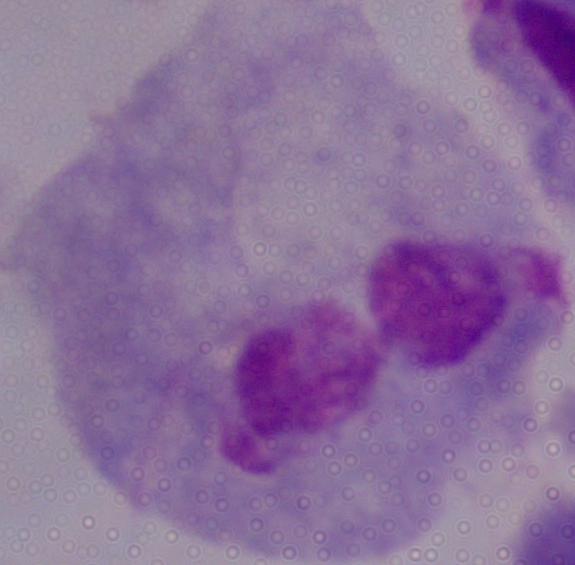

Summary:
  - Magnification: 1000x
  - Modality: micrograph
  - Identification: trichomonad